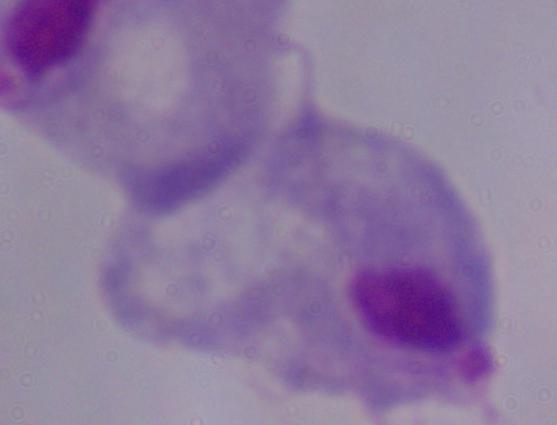

Summary:
  - Identification: trichomonad
  - Modality: photomicrograph
  - Magnification: 1000x